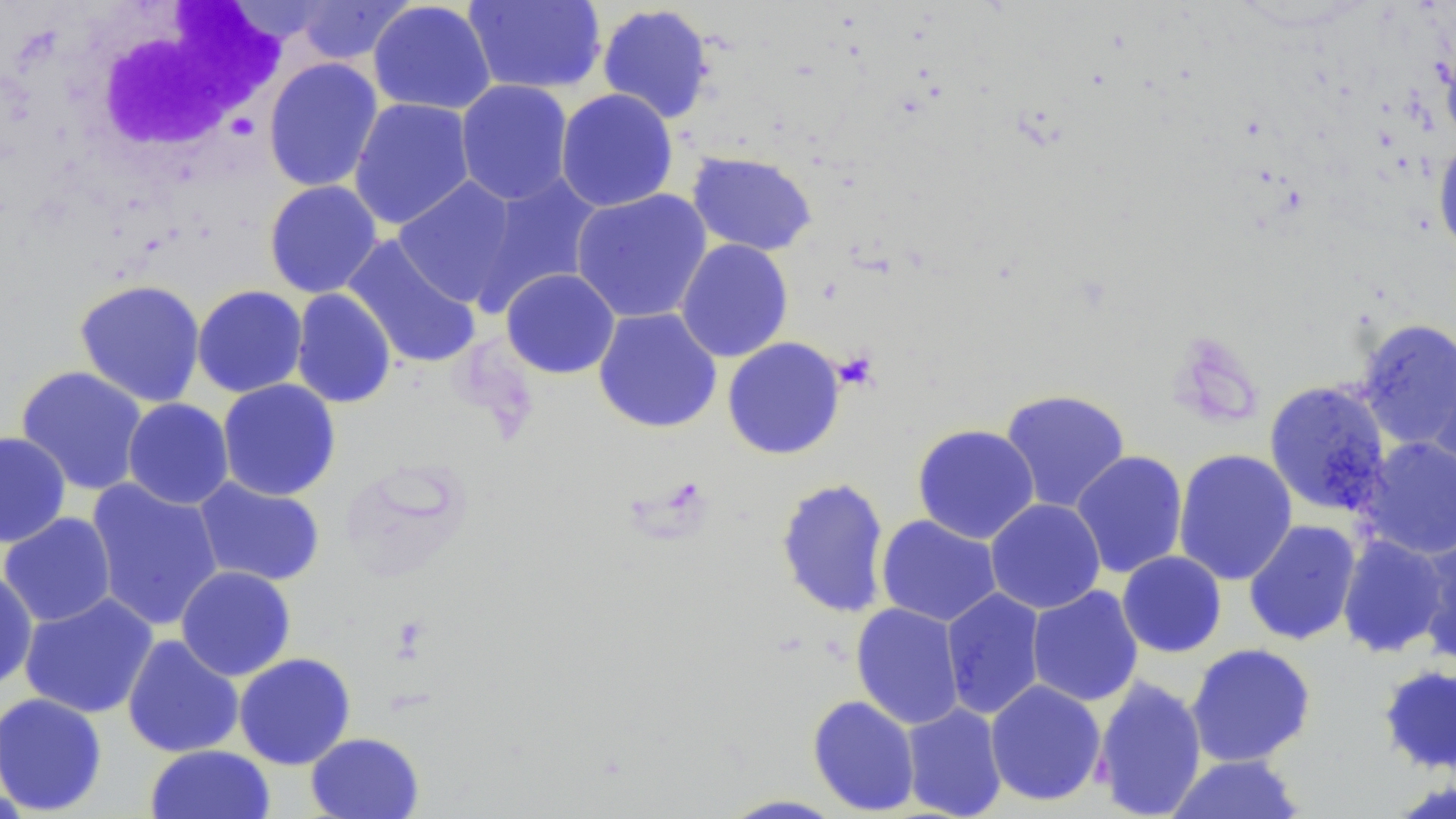
Summary:
  - Coordinate format: approximate bounding boxes as named x1/y1/x2/y2 corners in pixels
  - Uninfected red blood cell locations: (x1=292, y1=0, x2=415, y2=65), (x1=463, y1=0, x2=606, y2=95), (x1=226, y1=1, x2=335, y2=45), (x1=368, y1=1, x2=496, y2=115), (x1=596, y1=4, x2=715, y2=124), (x1=1440, y1=39, x2=1456, y2=148), (x1=263, y1=57, x2=383, y2=192), (x1=455, y1=79, x2=574, y2=206), (x1=555, y1=88, x2=678, y2=212), (x1=349, y1=97, x2=475, y2=230), (x1=1433, y1=137, x2=1456, y2=258), (x1=686, y1=151, x2=818, y2=256), (x1=473, y1=173, x2=604, y2=308), (x1=392, y1=177, x2=521, y2=307), (x1=263, y1=180, x2=383, y2=298), (x1=571, y1=189, x2=713, y2=323), (x1=341, y1=236, x2=483, y2=370), (x1=675, y1=238, x2=794, y2=362), (x1=500, y1=268, x2=620, y2=379), (x1=74, y1=278, x2=206, y2=408), (x1=192, y1=285, x2=308, y2=398), (x1=290, y1=288, x2=397, y2=409), (x1=592, y1=307, x2=723, y2=434), (x1=1355, y1=318, x2=1456, y2=453), (x1=722, y1=337, x2=846, y2=460), (x1=1427, y1=349, x2=1456, y2=487), (x1=15, y1=365, x2=149, y2=496), (x1=217, y1=379, x2=342, y2=501), (x1=1263, y1=380, x2=1392, y2=517), (x1=999, y1=389, x2=1131, y2=513), (x1=122, y1=398, x2=234, y2=510), (x1=911, y1=424, x2=1040, y2=544), (x1=0, y1=431, x2=71, y2=548), (x1=1357, y1=436, x2=1456, y2=560), (x1=1173, y1=449, x2=1298, y2=586), (x1=1070, y1=450, x2=1189, y2=579), (x1=192, y1=476, x2=326, y2=587), (x1=774, y1=477, x2=892, y2=619), (x1=85, y1=479, x2=225, y2=631), (x1=985, y1=498, x2=1106, y2=614), (x1=1, y1=512, x2=117, y2=627), (x1=876, y1=515, x2=1002, y2=627), (x1=1243, y1=519, x2=1362, y2=646), (x1=1416, y1=527, x2=1456, y2=667), (x1=1336, y1=534, x2=1451, y2=658), (x1=1117, y1=551, x2=1227, y2=658), (x1=0, y1=566, x2=39, y2=691), (x1=175, y1=566, x2=296, y2=681), (x1=1026, y1=585, x2=1144, y2=706), (x1=940, y1=588, x2=1047, y2=720), (x1=19, y1=592, x2=158, y2=719), (x1=850, y1=602, x2=965, y2=729), (x1=122, y1=634, x2=245, y2=758), (x1=1185, y1=642, x2=1317, y2=767), (x1=234, y1=652, x2=356, y2=769), (x1=1378, y1=664, x2=1456, y2=775), (x1=1091, y1=675, x2=1208, y2=819), (x1=985, y1=679, x2=1107, y2=807), (x1=0, y1=693, x2=108, y2=816), (x1=807, y1=695, x2=921, y2=816), (x1=901, y1=702, x2=1007, y2=818), (x1=305, y1=731, x2=425, y2=818), (x1=144, y1=744, x2=276, y2=819), (x1=1165, y1=754, x2=1307, y2=818), (x1=717, y1=794, x2=848, y2=818)
  - White blood cell locations: (x1=61, y1=2, x2=288, y2=177)
  - Slide-level diagnosis: negative for blood parasites
  - Preparation: thin blood smear
  - Modality: optical microscopy
  - Image size: 1456×819 pixels
  - Field of view: single
  - Stain: May-Grünwald-Giemsa
  - Magnification: 1000x